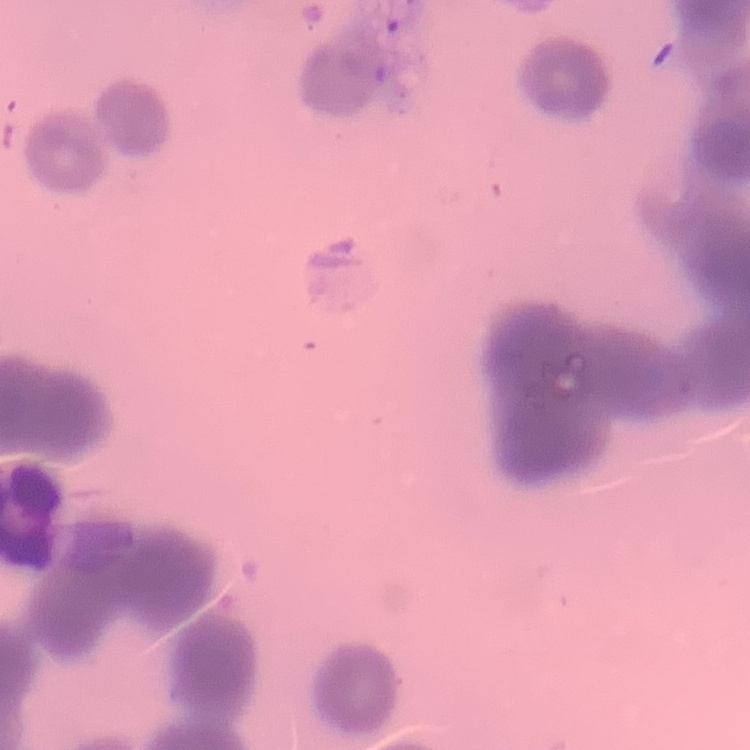

The red blood cells exhibit rouleaux formation. Stained with either Field's or Giemsa. One tile cut from a larger photomicrograph. Thin blood film.